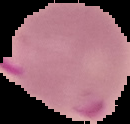

image size = 130×124 pixels
image type = cell region segmented out of the field of view; surrounding area masked to black
preparation = thin blood smear
result = malaria parasites detected